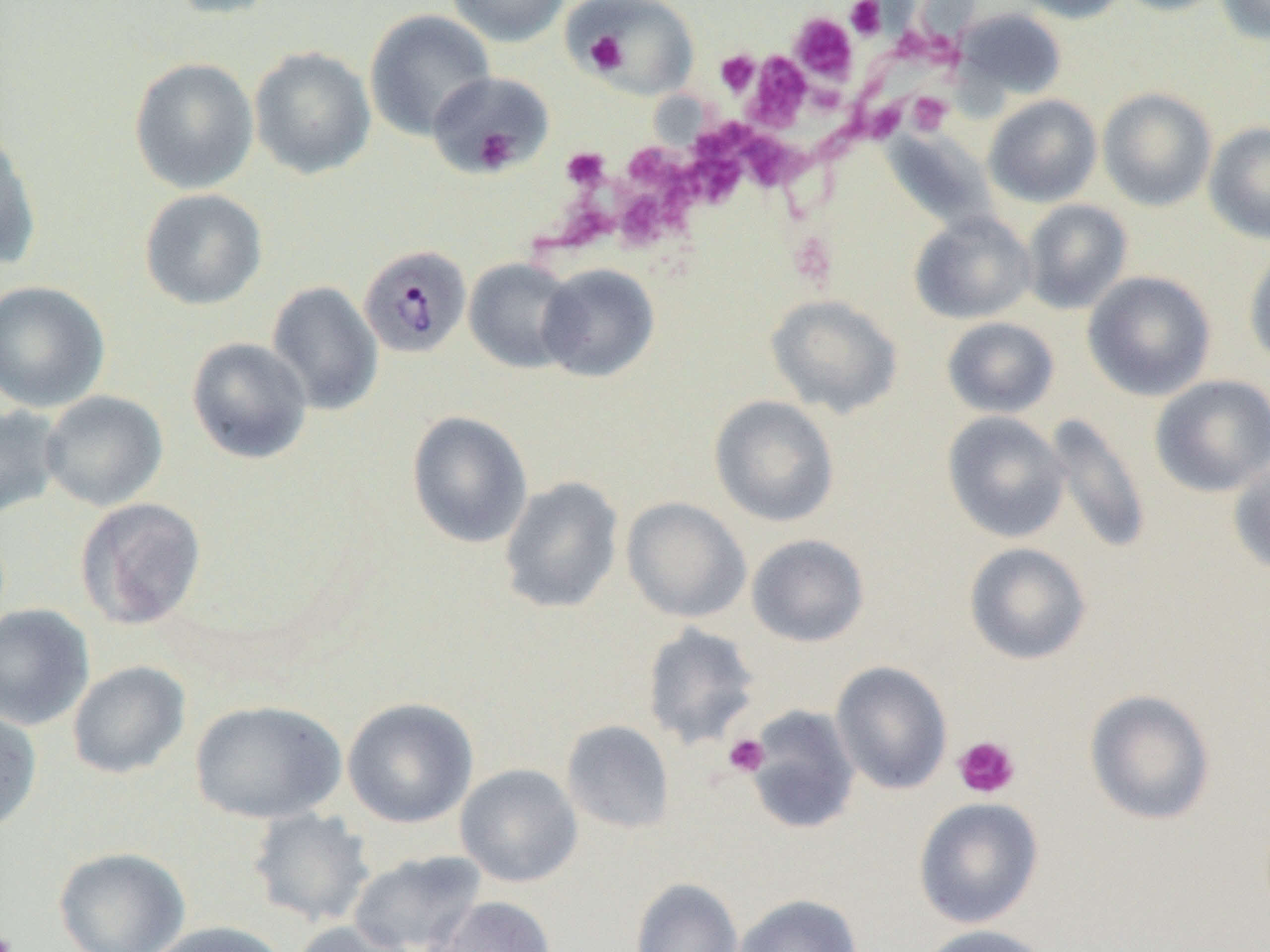
Approximate bounding boxes as (x1,y1)-(x2,y2) corner pairs in pixels. Plasmodium malariae-infected red blood cell locations: (358,245)-(472,358). Platelet locations: (845,0)-(886,40), (789,12)-(858,83), (577,21)-(648,79), (895,32)-(956,63), (584,33)-(628,75), (714,49)-(760,97), (745,53)-(811,131), (816,80)-(856,111), (907,91)-(953,136), (856,98)-(906,144), (692,116)-(757,170), (812,121)-(855,175), (474,128)-(518,172), (739,131)-(805,193), (623,141)-(679,191), (561,147)-(610,191), (685,151)-(746,210), (614,189)-(671,251), (537,198)-(609,252), (790,240)-(838,287), (723,733)-(770,777), (953,735)-(1021,799), (0,923)-(20,952). Uninfected red blood cell locations: (161,0)-(287,20), (446,0)-(569,47), (1010,0)-(1130,23), (1112,0)-(1230,16), (1215,0)-(1270,45), (574,1)-(698,99), (955,8)-(1066,100), (364,9)-(496,141), (249,46)-(376,180), (129,57)-(258,194), (427,71)-(553,175), (1097,87)-(1217,211), (983,95)-(1103,207), (0,121)-(43,269), (1204,121)-(1270,245), (881,129)-(997,229), (139,188)-(268,310), (1021,199)-(1132,315), (909,211)-(1036,325), (1244,245)-(1270,370), (464,258)-(579,373), (536,263)-(660,382), (1083,270)-(1216,401), (0,280)-(110,413), (266,281)-(383,416), (765,294)-(903,418), (941,317)-(1060,418), (186,336)-(313,465), (1149,374)-(1270,498), (39,390)-(168,511), (708,395)-(841,528), (0,403)-(64,521), (407,411)-(533,548), (942,411)-(1069,543), (1042,413)-(1153,556), (1228,460)-(1270,576), (498,476)-(624,614), (74,497)-(207,630), (621,497)-(751,623), (746,534)-(870,647), (963,542)-(1092,665), (0,603)-(95,730), (641,623)-(761,750), (831,660)-(953,794), (67,661)-(191,779), (1084,689)-(1216,826), (342,697)-(479,829), (190,699)-(347,824), (744,704)-(861,835), (0,706)-(43,835), (561,720)-(675,835), (455,763)-(583,888), (914,797)-(1044,928), (247,807)-(376,927), (53,846)-(190,952), (348,849)-(487,952), (630,877)-(744,952), (731,894)-(863,952), (426,895)-(557,952), (146,920)-(291,952), (289,920)-(418,952), (915,924)-(1055,952). Slide-level diagnosis: Plasmodium malariae. Thin blood smear. Single field of view. Captured at 1000x magnification. Image is 1270×952 pixels. Light microscopy.